Locate every uninfected red blood cell.
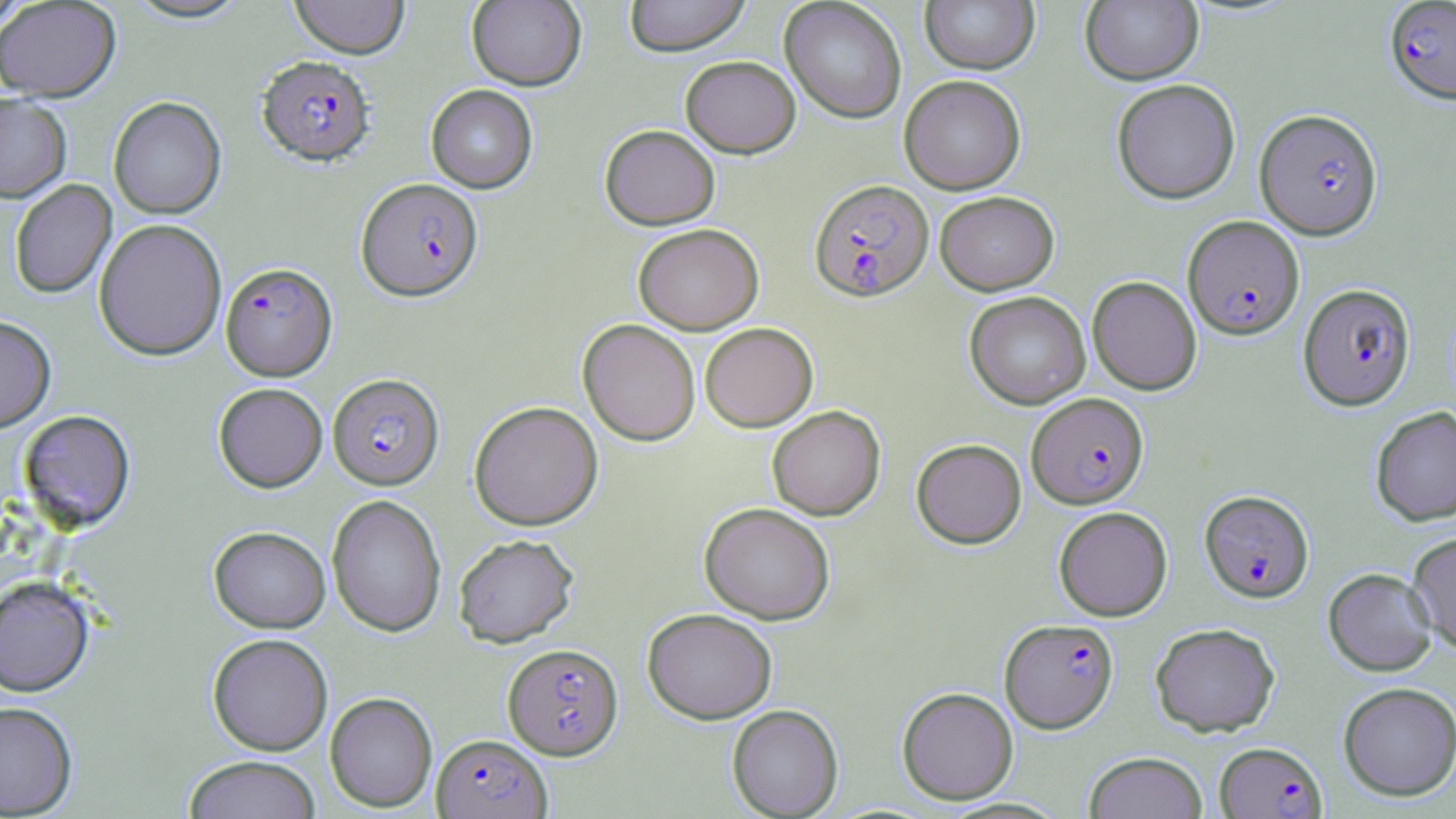
Approximate bounding boxes as [x1, y1, x2, y2] in pixels.
Uninfected red blood cells: [124, 0, 251, 25], [289, 0, 410, 59], [467, 0, 586, 91], [624, 0, 751, 56], [780, 0, 907, 123], [920, 0, 1040, 74], [0, 1, 34, 31], [0, 1, 121, 103], [1081, 1, 1203, 85], [680, 55, 801, 158], [899, 75, 1026, 194], [1111, 79, 1241, 204], [426, 85, 538, 193], [0, 94, 72, 204], [108, 97, 226, 220], [600, 125, 720, 230], [10, 180, 117, 299], [934, 191, 1059, 295], [93, 218, 228, 361], [633, 223, 763, 334], [1087, 276, 1202, 395], [964, 291, 1091, 409], [0, 316, 56, 433], [578, 319, 700, 446], [700, 322, 818, 431], [213, 382, 327, 493], [469, 401, 603, 531], [767, 405, 886, 521], [1371, 406, 1456, 526], [18, 410, 136, 533], [911, 438, 1026, 548], [327, 494, 446, 637], [699, 502, 835, 624], [1053, 506, 1173, 621], [209, 526, 331, 633], [1407, 532, 1456, 654], [453, 533, 579, 647], [1323, 568, 1437, 676], [0, 578, 94, 698], [642, 608, 777, 724], [1150, 622, 1280, 737], [207, 634, 333, 756], [1338, 682, 1456, 801], [897, 686, 1019, 804], [325, 692, 437, 813], [0, 702, 78, 817], [727, 704, 843, 818], [1083, 752, 1208, 819], [183, 756, 321, 819].

{
  "slide_level_diagnosis": "Plasmodium falciparum",
  "image_size": "1456×819 pixels",
  "modality": "light microscopy",
  "stain": "May-Grünwald-Giemsa",
  "preparation": "thin blood film",
  "magnification": "1000x",
  "field_of_view": "single",
  "plasmodium_falciparum_infected_red_blood_cell_locations": "approximate bounding boxes as [x1, y1, x2, y2] in pixels: [1384, 0, 1456, 104], [256, 56, 376, 167], [1255, 108, 1382, 239], [356, 178, 483, 303], [809, 179, 933, 301], [1183, 215, 1304, 339], [221, 263, 337, 381], [1298, 283, 1416, 410], [328, 374, 444, 490], [1027, 393, 1148, 508], [1199, 490, 1314, 602], [1000, 618, 1118, 733], [503, 643, 623, 759], [431, 734, 551, 819], [1215, 740, 1327, 818]"
}